Locate every Plasmodium falciparum-infected red blood cell.
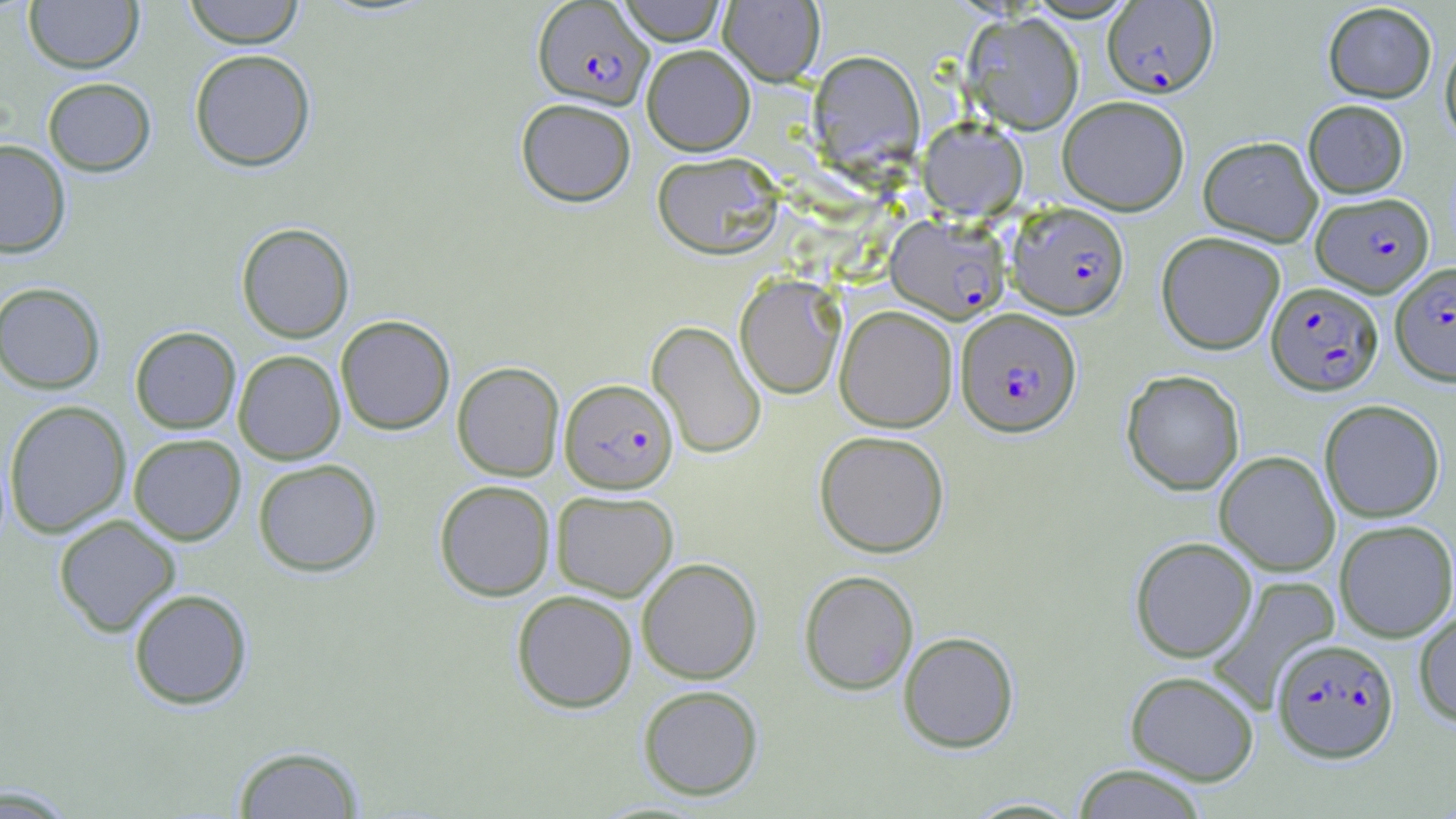

Approximate bounding boxes as named x1/y1/x2/y2 corners in pixels.
Plasmodium falciparum-infected red blood cells: (x1=532, y1=0, x2=653, y2=109), (x1=1102, y1=1, x2=1218, y2=98), (x1=1311, y1=191, x2=1433, y2=297), (x1=1006, y1=202, x2=1130, y2=319), (x1=886, y1=214, x2=1010, y2=324), (x1=1390, y1=263, x2=1456, y2=385), (x1=1266, y1=281, x2=1384, y2=395), (x1=957, y1=308, x2=1081, y2=436), (x1=563, y1=386, x2=681, y2=501), (x1=1271, y1=638, x2=1399, y2=762).

Summary:
  - Uninfected red blood cell locations: (x1=24, y1=0, x2=144, y2=74), (x1=183, y1=0, x2=305, y2=48), (x1=615, y1=0, x2=728, y2=45), (x1=718, y1=0, x2=824, y2=86), (x1=1322, y1=2, x2=1437, y2=103), (x1=1314, y1=3, x2=1417, y2=196), (x1=963, y1=12, x2=1084, y2=134), (x1=1440, y1=38, x2=1456, y2=148), (x1=641, y1=44, x2=755, y2=155), (x1=189, y1=49, x2=316, y2=171), (x1=809, y1=51, x2=924, y2=170), (x1=42, y1=77, x2=156, y2=176), (x1=1057, y1=95, x2=1190, y2=215), (x1=515, y1=98, x2=637, y2=206), (x1=1303, y1=100, x2=1408, y2=198), (x1=918, y1=118, x2=1028, y2=220), (x1=1198, y1=135, x2=1322, y2=246), (x1=0, y1=139, x2=71, y2=258), (x1=651, y1=152, x2=783, y2=258), (x1=236, y1=222, x2=354, y2=343), (x1=1156, y1=231, x2=1285, y2=355), (x1=735, y1=275, x2=845, y2=399), (x1=0, y1=282, x2=106, y2=394), (x1=835, y1=305, x2=958, y2=432), (x1=335, y1=315, x2=455, y2=435), (x1=647, y1=322, x2=766, y2=459), (x1=129, y1=326, x2=241, y2=434), (x1=233, y1=350, x2=346, y2=464), (x1=452, y1=361, x2=564, y2=480), (x1=1121, y1=369, x2=1245, y2=495), (x1=1319, y1=399, x2=1445, y2=523), (x1=4, y1=400, x2=131, y2=538), (x1=814, y1=430, x2=950, y2=557), (x1=128, y1=433, x2=245, y2=545), (x1=1215, y1=451, x2=1340, y2=576), (x1=252, y1=459, x2=381, y2=577), (x1=434, y1=479, x2=556, y2=601), (x1=551, y1=490, x2=678, y2=601), (x1=53, y1=514, x2=181, y2=637), (x1=1334, y1=519, x2=1456, y2=641), (x1=1130, y1=537, x2=1257, y2=662), (x1=636, y1=557, x2=762, y2=684), (x1=798, y1=569, x2=919, y2=695), (x1=1207, y1=575, x2=1341, y2=705), (x1=128, y1=589, x2=253, y2=709), (x1=511, y1=589, x2=638, y2=713), (x1=1413, y1=608, x2=1456, y2=727), (x1=898, y1=631, x2=1019, y2=752), (x1=1125, y1=670, x2=1260, y2=785), (x1=637, y1=684, x2=764, y2=800), (x1=230, y1=744, x2=366, y2=818), (x1=1072, y1=764, x2=1210, y2=819), (x1=0, y1=784, x2=82, y2=816), (x1=961, y1=797, x2=1087, y2=818)
  - Slide-level diagnosis: Plasmodium falciparum
  - Stain: May-Grünwald-Giemsa
  - Image size: 1456×819 pixels
  - Modality: optical microscopy
  - Magnification: 1000x
  - Preparation: thin blood smear
  - Field of view: one of a larger specimen